Name the parasite shown.
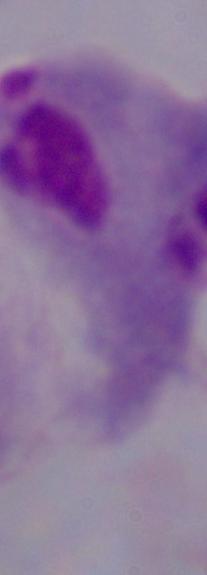
This is a trichomonad.

1000x magnification. Photomicrograph.